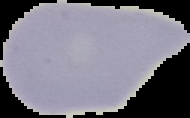

preparation = thin blood film
result = no Plasmodium parasites seen
image size = 190×118 pixels
image type = segmented cell region with the area outside set to black